Name the parasite shown.
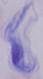

A trypanosome.

Summary:
  - Magnification: 1000x
  - Modality: micrograph